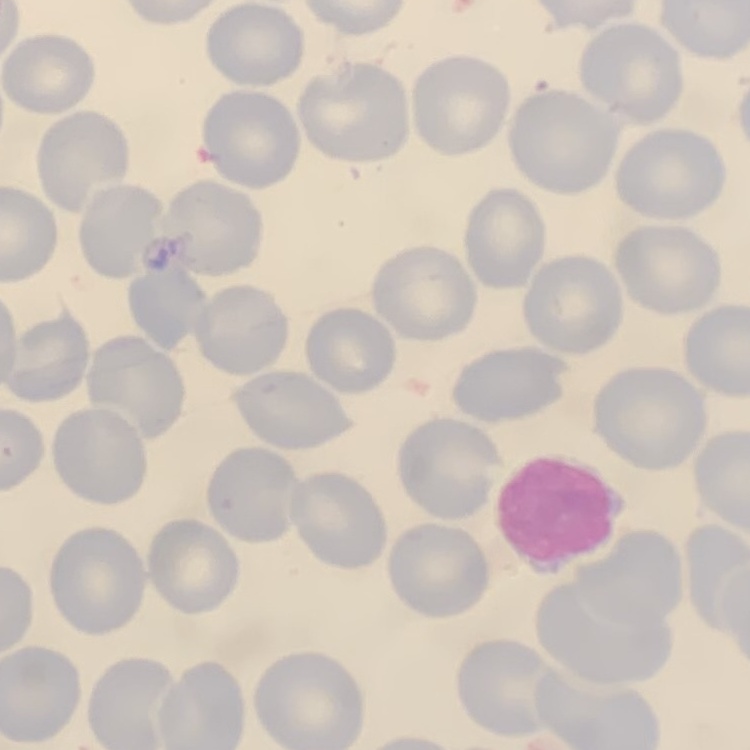 The erythrocytes show no rouleaux formation. One tile cut from a larger photomicrograph. Field's or Giemsa stain. Thin blood smear.